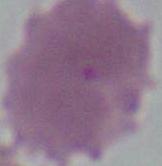

identification: red blood cell
magnification: 1000x
modality: photomicrograph